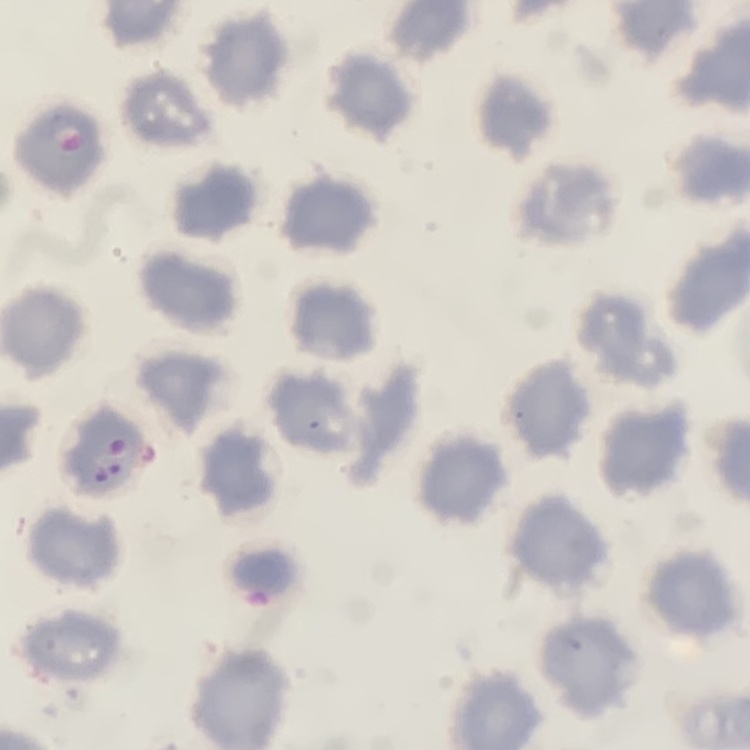
erythrocyte_morphology: no rouleaux formation
image_type: one tile cut from a larger photomicrograph
preparation: thin peripheral smear
stain: Field's or Giemsa